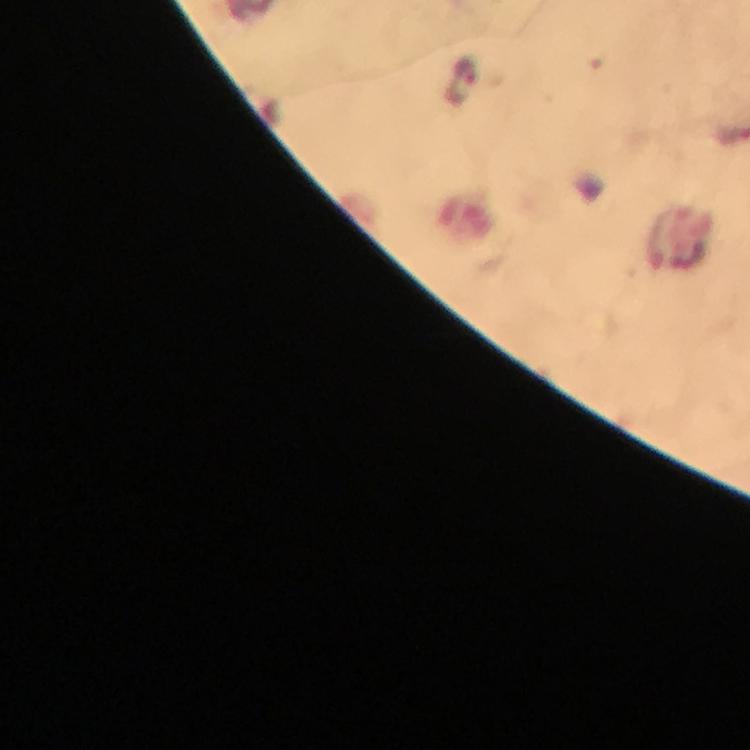

Approximate centers as (x, y) in pixels. Plasmodium parasite locations: (462, 84). Thick blood film. Giemsa-stained preparation. From a diagnostic examination for malaria. Photographed with a smartphone mounted on the microscope. Cropped region of a single field of view. 100x magnification. Image is 750×750 pixels. Immersion oil applied.